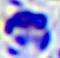

identification = white blood cell
magnification = 400x
modality = micrograph